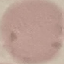

Result: no malaria parasites seen. Thin blood smear. Photographed with a smartphone camera at the microscope eyepiece. Giemsa-stained preparation. Cell patch, automatically extracted from a larger field of view and resized to 64 × 64 pixels.